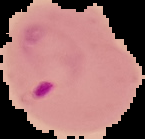

Summary:
  - Image size: 145×139 pixels
  - Result: Plasmodium parasites detected
  - Preparation: thin blood film
  - Image type: segmented cell region with the area outside set to black